Comment on the morphology of the erythrocytes.
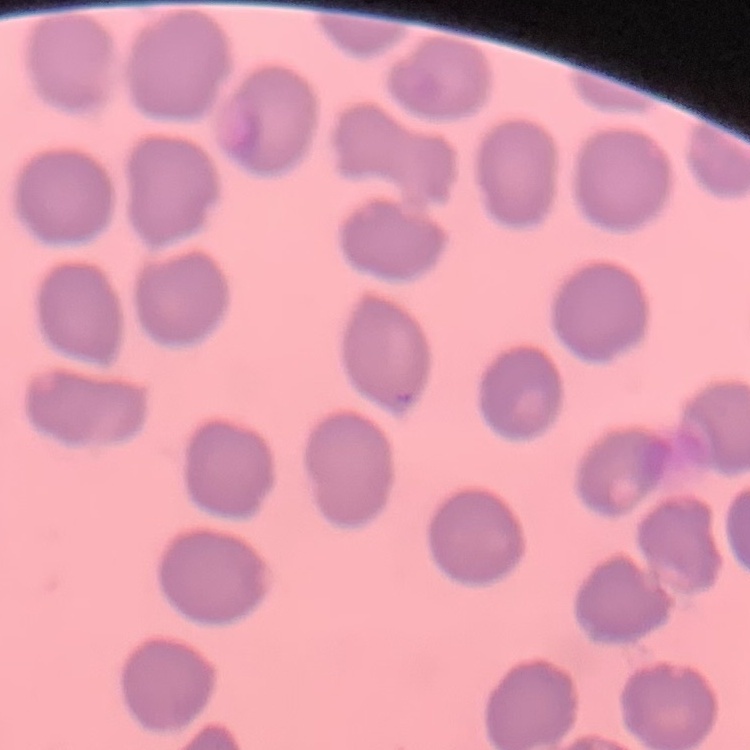

They show no rouleaux formation.

Thin peripheral smear. Square crop of a larger photomicrograph. Field's or Giemsa stain.